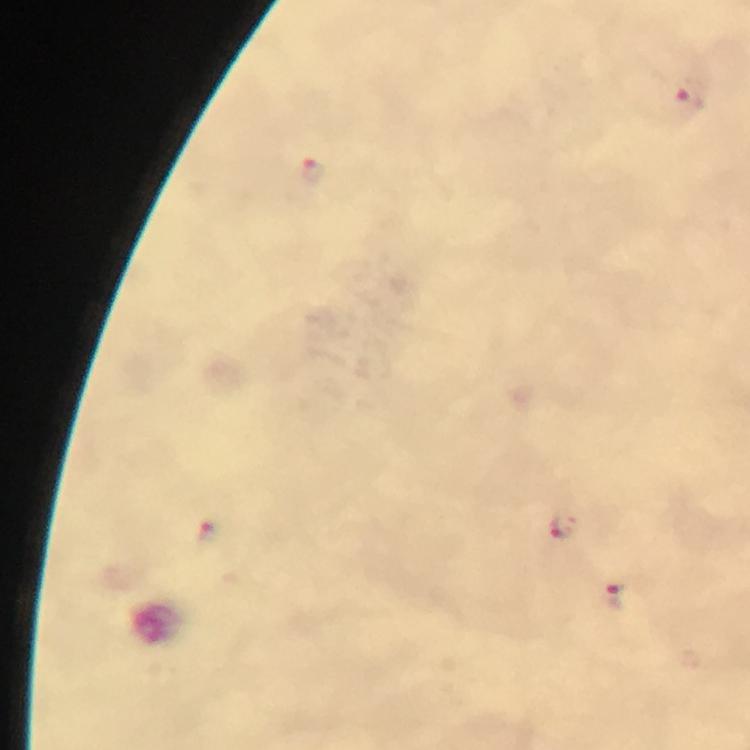

Approximate centers as [x, y] in pixels. Malaria parasite locations: [313, 168], [565, 527], [210, 532], [613, 596]. Photographed through the microscope with a smartphone camera. Immersion oil was used. A crop from one field of view. Thick blood smear. Image is 750×750 pixels. 100x magnification. Giemsa stain. From a malaria diagnostic workup.